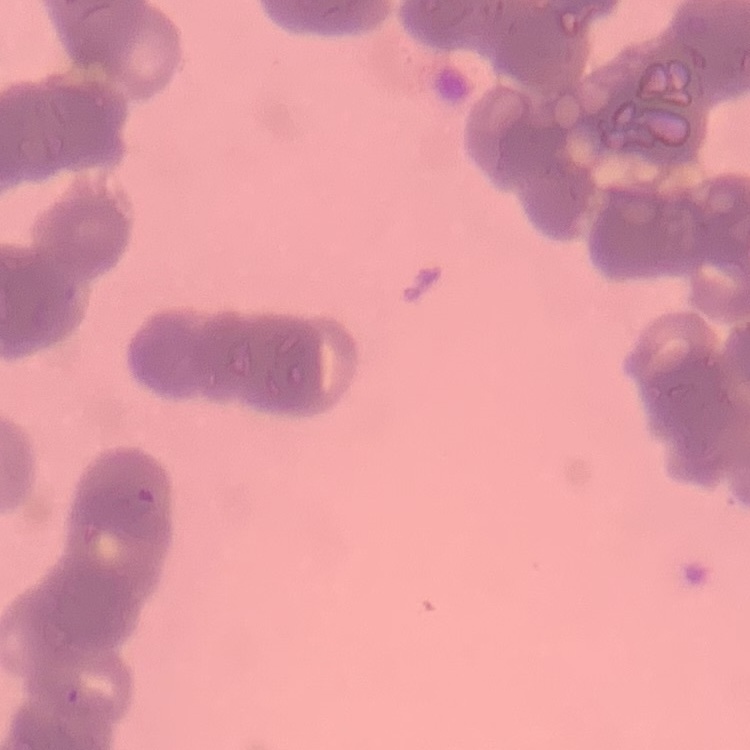

Summary:
  - Red blood cell morphology: rouleaux formation
  - Preparation: thin blood smear
  - Stain: Field's or Giemsa
  - Image type: one tile cut from a larger photomicrograph